Give the position of every leukocyte visible.
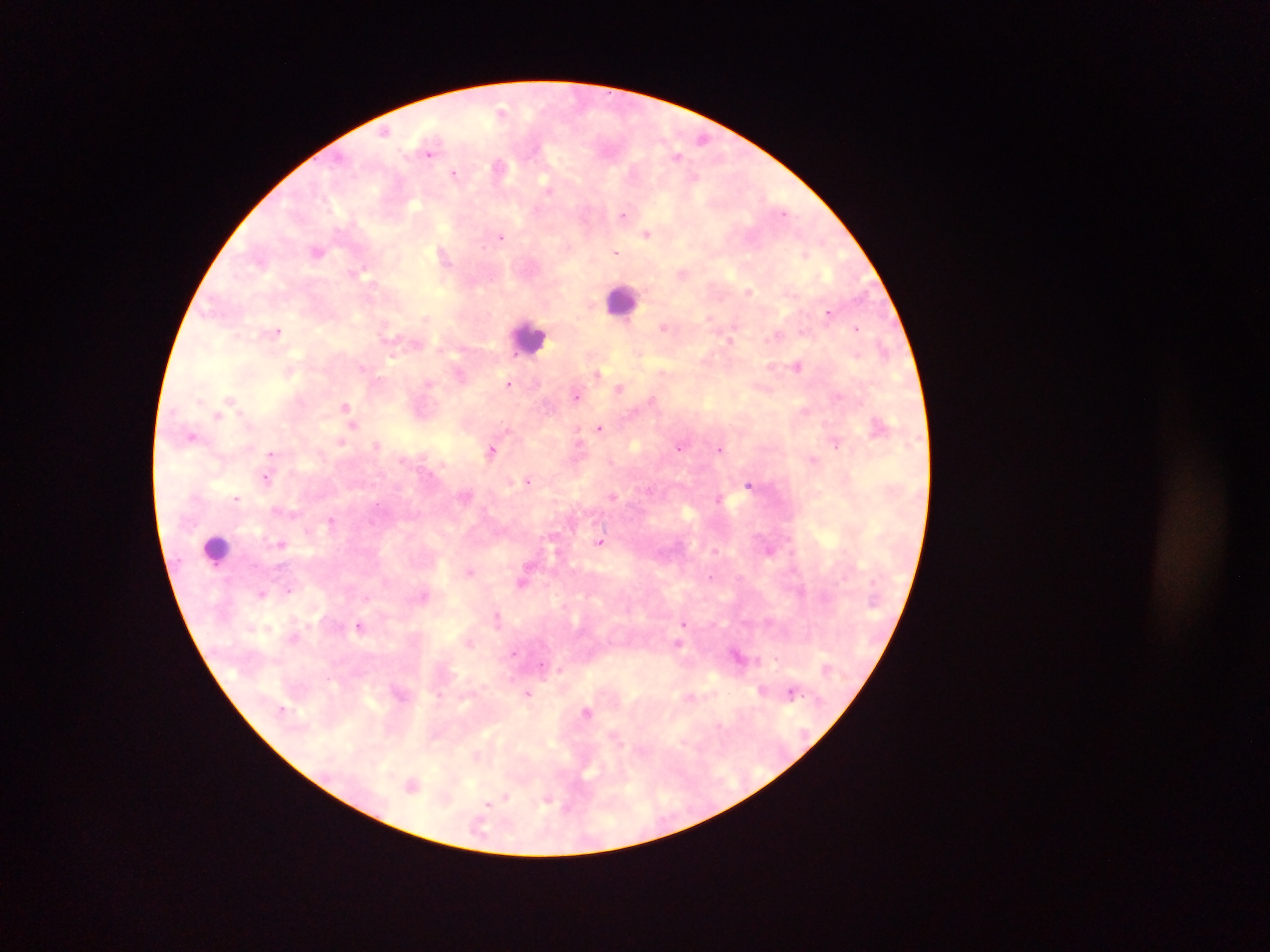

Approximate centers as (x, y) in pixels.
Leukocytes: (622, 299), (529, 337), (216, 549).

Summary:
  - Plasmodium parasite locations: (502, 112), (386, 130), (703, 138), (430, 149), (677, 155), (499, 167), (455, 174), (624, 214), (647, 233), (501, 236), (317, 251), (615, 251), (445, 253), (805, 254), (683, 273), (749, 290), (829, 312), (711, 316), (664, 328), (857, 328), (276, 329), (777, 335), (732, 339), (798, 365), (288, 368), (597, 374), (509, 383), (620, 387), (577, 396), (231, 399), (347, 407), (217, 415), (354, 424), (880, 425), (600, 428), (193, 435), (341, 441), (836, 443), (376, 445), (680, 446), (720, 448), (492, 449), (271, 453), (814, 460), (267, 478), (528, 480), (749, 485), (466, 496), (612, 496), (237, 497), (720, 499), (275, 509), (331, 521), (601, 542), (281, 543), (769, 549), (470, 572), (523, 580), (290, 588), (262, 593), (498, 617), (685, 623), (361, 625), (267, 628), (294, 638), (470, 641), (678, 644), (513, 653), (738, 655), (560, 670), (763, 689), (528, 693), (791, 693), (587, 711), (412, 784), (505, 798), (547, 799), (489, 804)
  - Country: Ghana
  - Image size: 1270×952 pixels
  - Field of view: single
  - Capture: mobile-phone photograph through a microscope
  - Preparation: thick blood smear